Give a bounding box for every parasitised red blood cell.
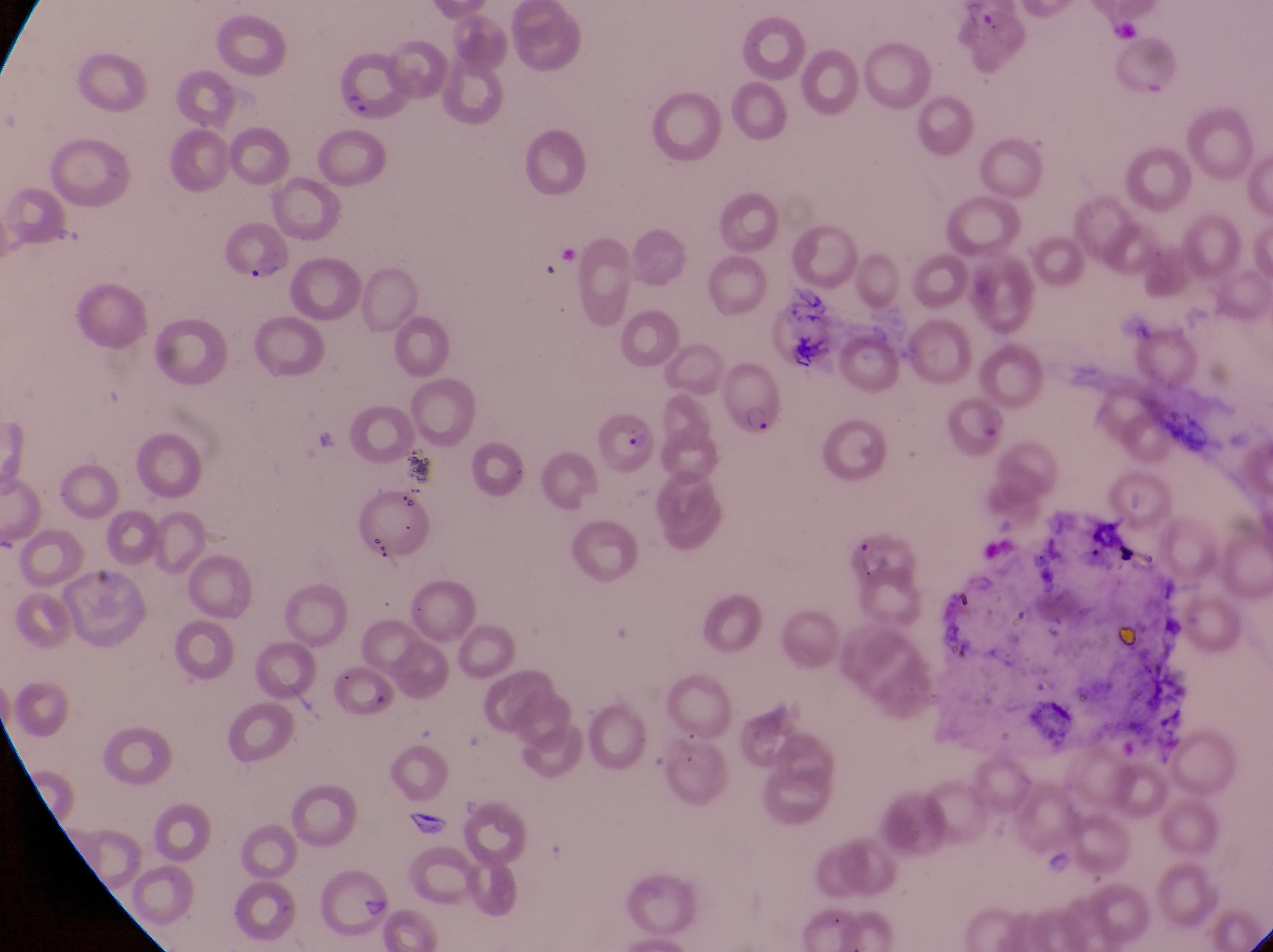
Approximate bounding boxes as [left, top, right, bottom] in pixels.
Parasitised red blood cells: [332, 55, 404, 118], [220, 223, 294, 280], [714, 352, 781, 439], [944, 398, 1011, 461], [601, 407, 656, 475].

Artifact (platelet-like body, stain precipitate, or debris) locations: [310, 415, 340, 457]. Image is 1273×952 pixels. Captured by a smartphone held over the eyepiece of an Olympus CX-23 microscope. Collected in Uganda. One field of view. Thin blood smear. At a magnification of 1000x.